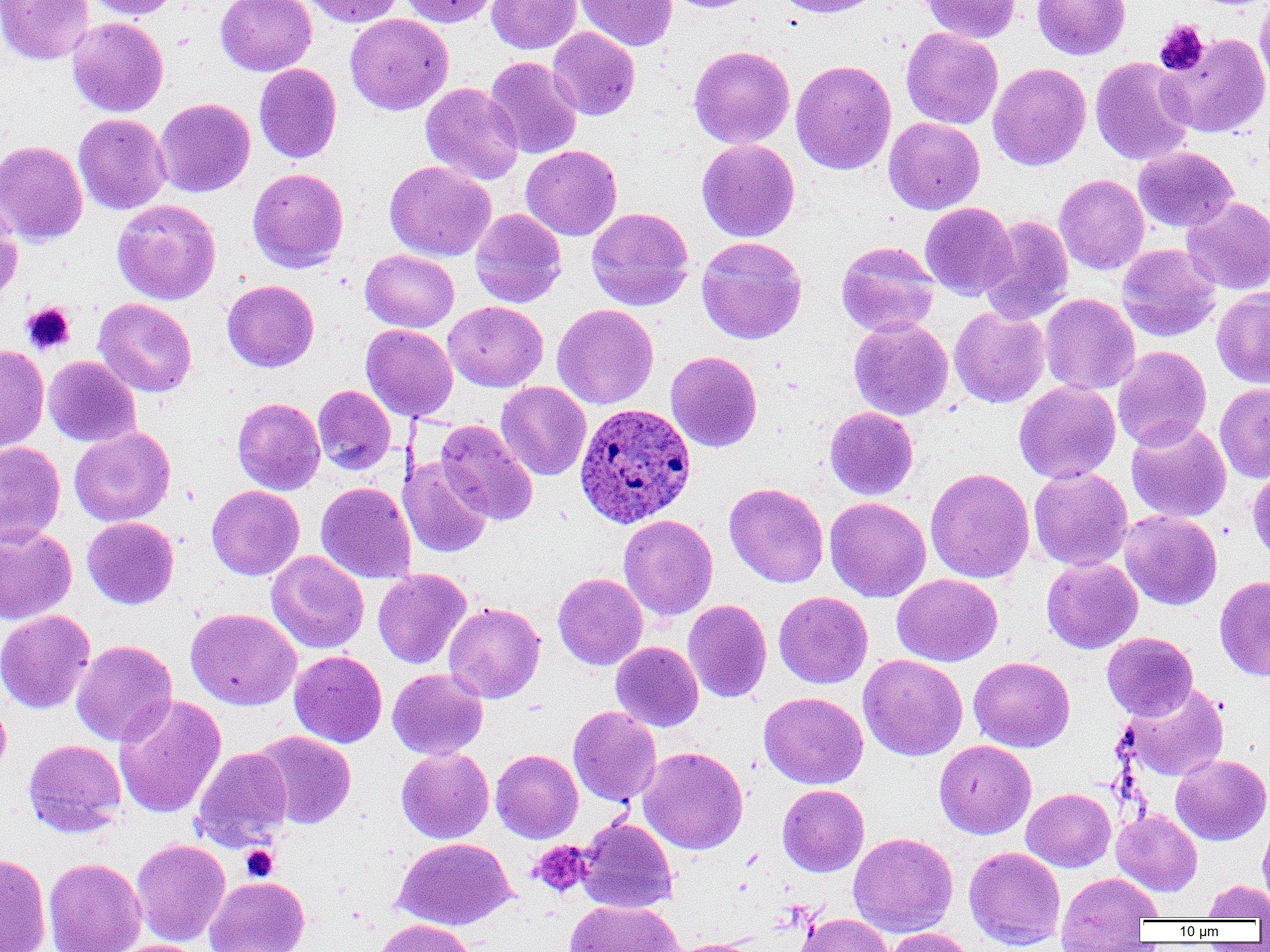
slide-level diagnosis = Plasmodium ovale
field of view = one of a larger specimen
platelet locations = approximate bounding boxes as (x1, y1, x2, y2) in pixels: (1154, 19, 1210, 76), (21, 303, 75, 355), (529, 840, 593, 898), (241, 845, 278, 882)
image size = 1270×952 pixels
preparation = thin blood film
Plasmodium ovale-infected red blood cell locations = approximate bounding boxes as (x1, y1, x2, y2) in pixels: (574, 403, 696, 528)
modality = light microscopy
magnification = 1000x
uninfected red blood cell locations = approximate bounding boxes as (x1, y1, x2, y2) in pixels: (1, 0, 94, 64), (84, 0, 180, 19), (215, 0, 316, 76), (302, 0, 404, 27), (398, 0, 500, 27), (487, 0, 581, 54), (575, 0, 677, 51), (660, 0, 764, 13), (772, 0, 885, 18), (918, 0, 1021, 44), (1032, 0, 1131, 60), (1255, 0, 1270, 96), (345, 13, 453, 115), (67, 17, 168, 117), (547, 27, 640, 120), (901, 28, 1003, 129), (1159, 32, 1270, 138), (688, 45, 795, 149), (484, 56, 582, 159), (1090, 57, 1195, 166), (790, 60, 896, 175), (988, 62, 1091, 171), (254, 63, 342, 164), (420, 83, 524, 185), (154, 98, 255, 197), (73, 113, 171, 215), (884, 117, 984, 214), (696, 139, 800, 242), (0, 140, 88, 246), (521, 145, 622, 241), (1133, 146, 1238, 233), (385, 160, 496, 261), (247, 168, 349, 272), (1054, 174, 1150, 275), (1182, 196, 1270, 295), (112, 199, 220, 305), (920, 202, 1018, 300), (0, 203, 22, 309), (586, 207, 694, 311), (470, 209, 566, 308), (979, 216, 1074, 324), (696, 236, 807, 344), (836, 241, 939, 337), (1117, 243, 1221, 342), (361, 249, 459, 332), (222, 280, 319, 372), (1212, 287, 1270, 389), (1040, 293, 1140, 395), (93, 298, 197, 397), (443, 301, 547, 391), (552, 304, 659, 409), (949, 306, 1050, 407), (849, 318, 953, 420), (361, 324, 458, 421), (0, 345, 49, 452), (1112, 346, 1212, 452), (665, 351, 762, 452), (43, 356, 141, 447), (496, 381, 591, 481), (1014, 381, 1120, 483), (1215, 383, 1270, 482), (313, 385, 395, 475), (232, 397, 325, 495), (825, 407, 918, 500), (435, 418, 538, 526), (1126, 421, 1231, 523), (69, 427, 175, 526), (0, 441, 65, 546), (399, 457, 492, 558), (1247, 464, 1270, 567), (1028, 467, 1133, 571), (925, 468, 1035, 583), (316, 482, 416, 583), (725, 482, 828, 588), (206, 485, 304, 580), (824, 496, 931, 602), (1119, 510, 1222, 610), (618, 514, 718, 621), (82, 517, 179, 610), (0, 526, 77, 624), (266, 551, 368, 654), (1042, 558, 1143, 654), (373, 569, 471, 669), (553, 573, 648, 670), (892, 574, 1003, 666), (1214, 575, 1270, 681), (774, 591, 873, 688), (683, 600, 772, 703), (443, 602, 545, 703), (185, 607, 301, 710), (0, 610, 95, 714), (1102, 632, 1198, 721), (71, 640, 177, 746), (611, 641, 703, 731), (289, 650, 387, 747), (858, 654, 967, 761), (968, 656, 1075, 752), (387, 668, 488, 760), (1121, 683, 1230, 782), (758, 691, 868, 789), (0, 694, 11, 778), (114, 695, 226, 819), (568, 706, 661, 806), (252, 731, 356, 829), (23, 739, 127, 837), (934, 740, 1036, 839), (638, 746, 748, 854), (192, 747, 293, 850), (395, 747, 494, 843), (491, 749, 583, 843), (1171, 754, 1269, 845), (777, 784, 869, 876), (1021, 788, 1116, 872), (1112, 809, 1202, 895), (576, 817, 677, 913), (1258, 817, 1270, 910), (847, 832, 958, 937), (394, 837, 516, 929), (131, 839, 231, 946), (964, 846, 1066, 949), (0, 854, 51, 952), (43, 857, 147, 952), (1056, 872, 1161, 948), (205, 876, 310, 952), (1201, 880, 1270, 920), (565, 899, 684, 952), (794, 913, 894, 952), (373, 918, 475, 952), (884, 927, 975, 952), (667, 938, 766, 952), (107, 939, 207, 952)